Classify the preparation.
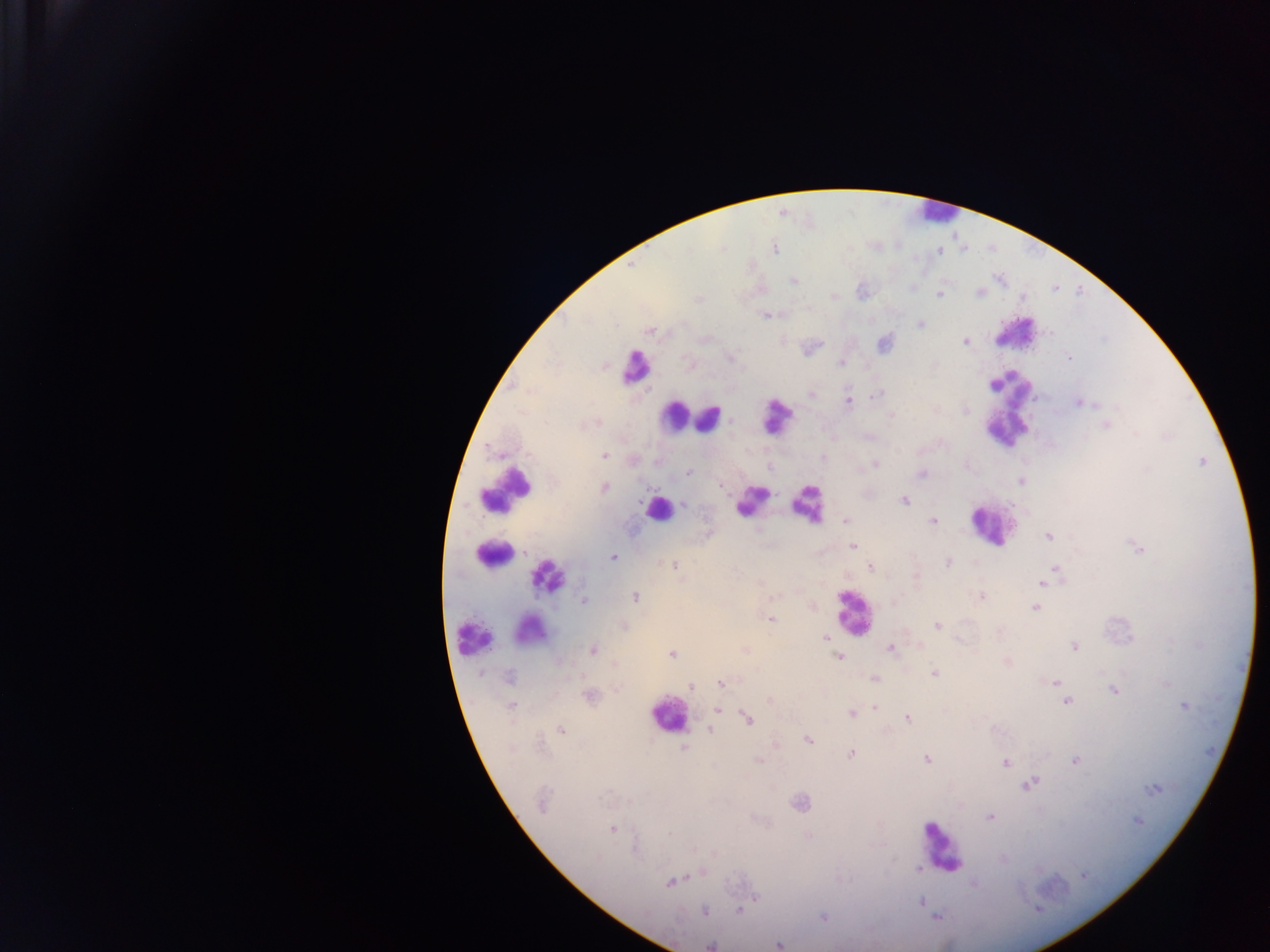

This is a thick smear.

Approximate centers as x y in pixels.
Summary:
  - Malaria parasite locations: 775 249; 940 251; 794 281; 980 293; 938 295; 766 316; 920 324; 649 331; 966 342; 884 344; 1069 357; 730 358; 841 363; 647 391; 812 395; 876 396; 848 401; 1079 403; 966 411; 891 416; 1106 426; 604 455; 823 457; 875 464; 688 474; 921 474; 1020 480; 721 485; 604 487; 904 501; 683 504; 845 521; 933 522; 1048 537; 853 547; 1138 548; 613 557; 948 563; 675 566; 870 567; 1056 569; 1042 583; 982 596; 636 597; 584 601; 1035 608; 771 620; 624 625; 937 626; 826 636; 1075 647; 890 648; 593 650; 745 650; 671 655; 839 657; 934 673; 509 677; 876 680; 1055 682; 721 683; 1166 683; 691 687; 1114 691; 591 696; 1066 702; 511 705; 1184 706; 875 707; 718 710; 852 714; 748 719; 907 719; 561 730; 710 730; 807 740; 685 748; 851 754; 926 759; 758 761; 1075 761; 1005 763; 1029 784; 1152 789; 542 803; 800 803; 989 817; 1138 821; 612 829; 917 870; 701 872; 1083 875; 670 883; 973 884; 753 898; 921 901; 704 911; 739 911; 936 917; 823 918; 711 945; 778 945
  - Leukocyte locations: 934 214; 1016 330; 634 374; 1009 409; 674 415; 708 418; 775 419; 506 487; 750 502; 808 503; 658 509; 990 525; 492 553; 547 573; 853 613; 523 631; 467 643; 667 715; 938 851
  - Image size: 1270×952 pixels
  - Country: Ghana
  - Field of view: single
  - Capture: mobile-phone photograph through a microscope